Describe the morphology of the erythrocytes.
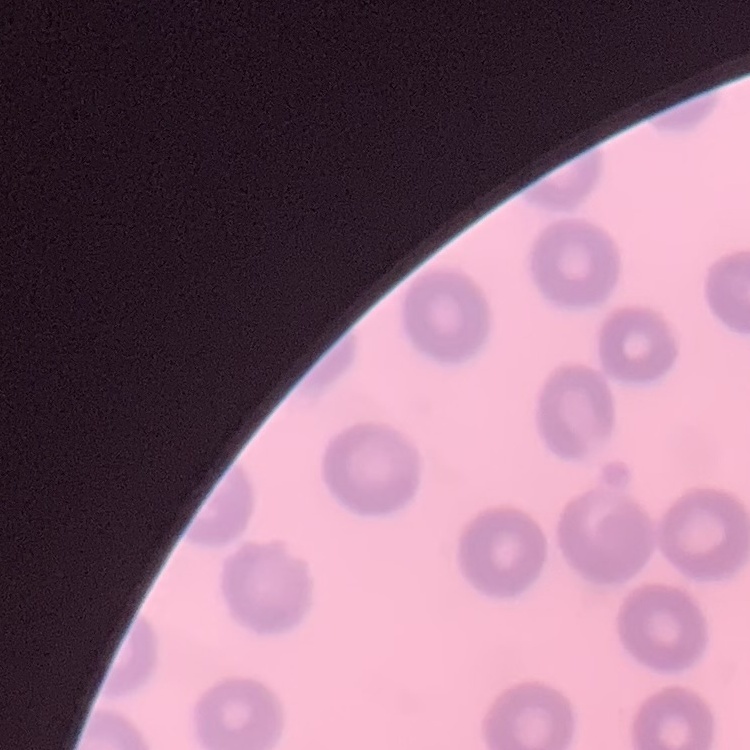
They show no rouleaux formation.

Square crop of a larger photomicrograph. Stained with either Field's or Giemsa. Thin blood film.